State which parasite is depicted.
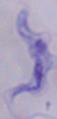
This is a trypanosome.

modality: micrograph
magnification: 1000x